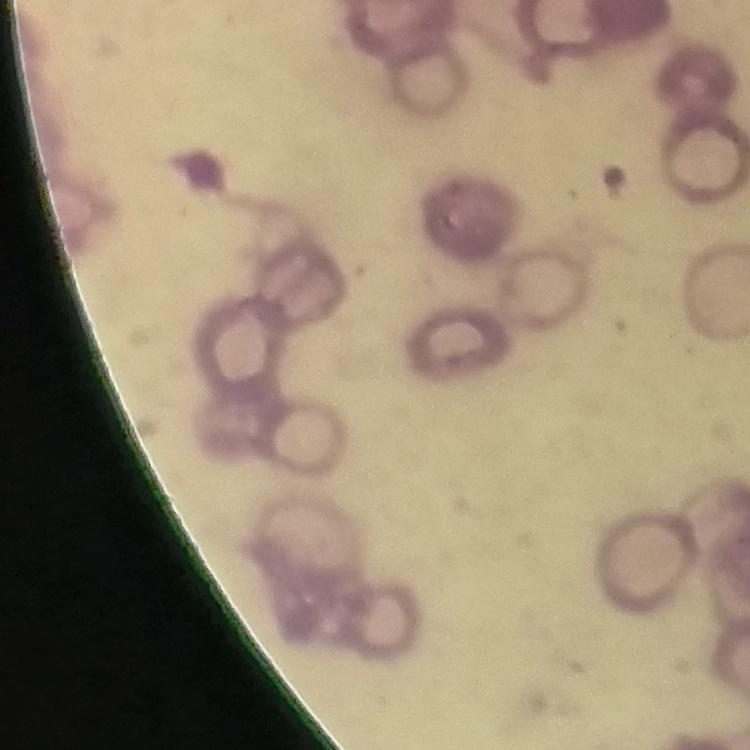
Summary:
  - Erythrocyte morphology: rouleaux formation
  - Stain: Field's or Giemsa
  - Preparation: thin peripheral smear
  - Image type: one tile cut from a larger photomicrograph